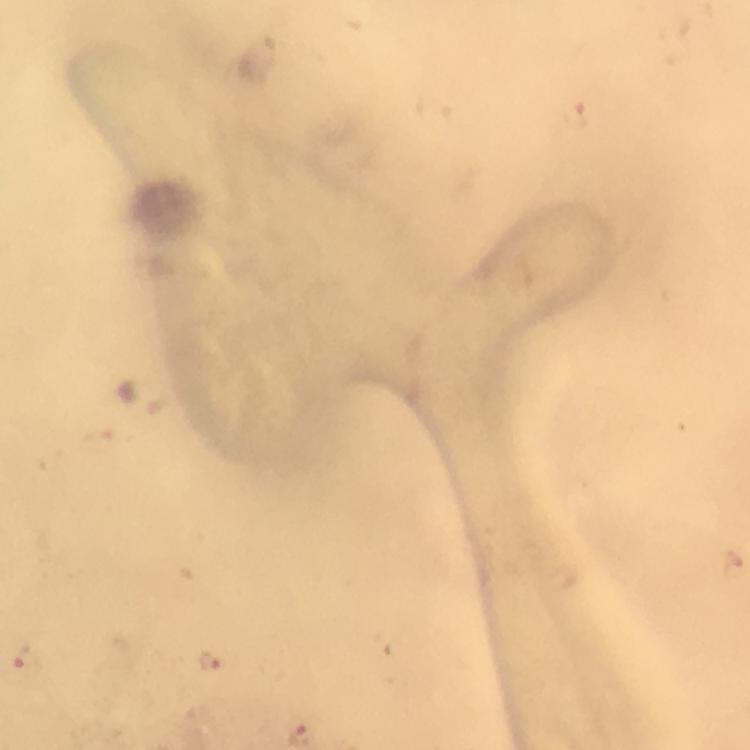
{
  "malaria_parasite_locations": "approximate centers as (x, y) in pixels: (212, 662), (24, 666)",
  "context": "from a diagnostic examination for malaria",
  "image_size": "750×750 pixels",
  "cropped_from": "one field of view",
  "capture": "smartphone camera through the microscope",
  "magnification": "100x",
  "preparation": "thick blood film",
  "immersion_oil": "used",
  "stain": "Giemsa"
}